Point out each Plasmodium parasite.
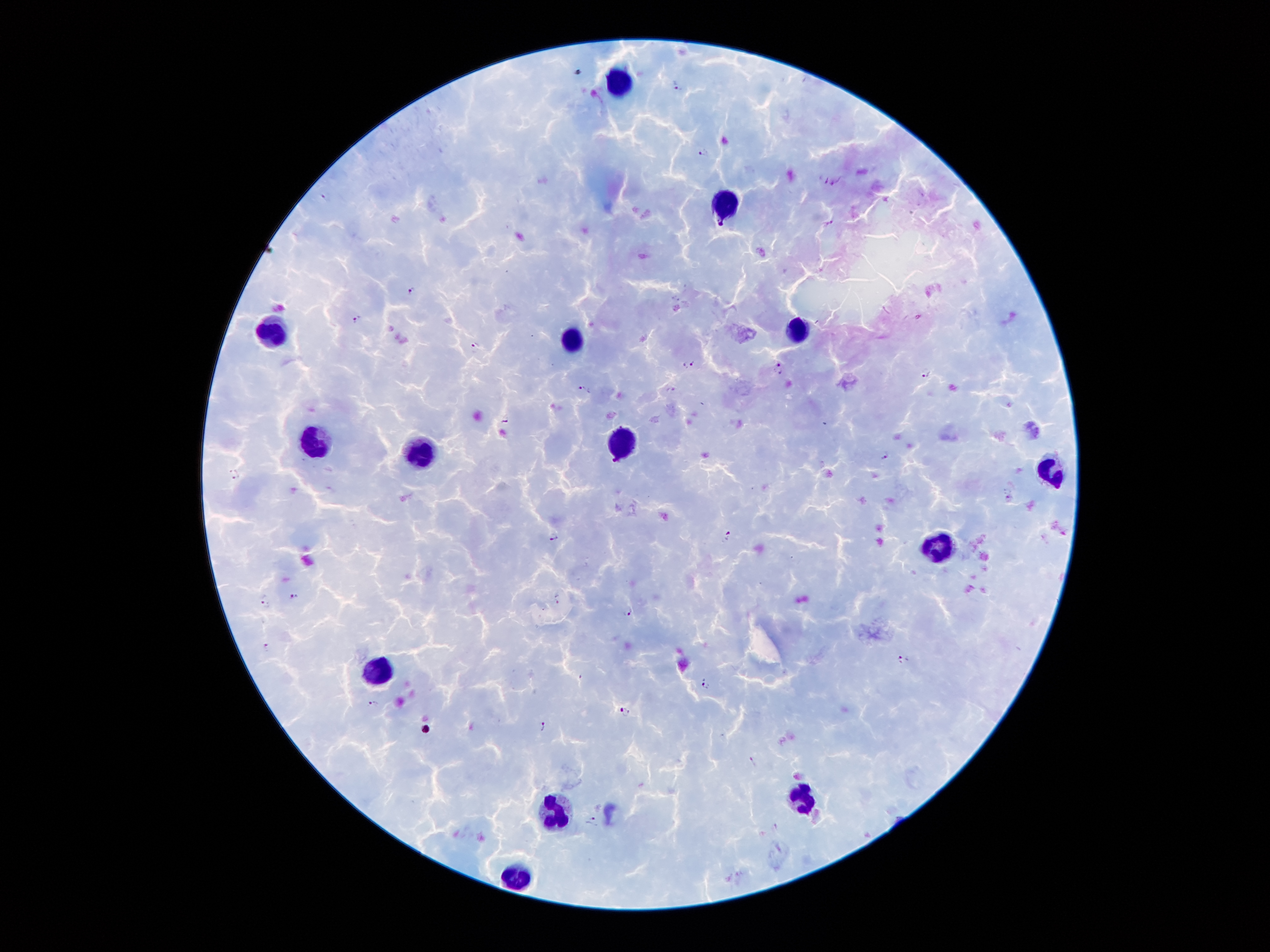

Approximate centers as {x, y} in pixels.
Plasmodium parasites: {676, 84}, {705, 152}, {822, 180}, {835, 182}, {327, 196}, {829, 222}, {411, 291}, {357, 319}, {475, 347}, {689, 364}, {780, 369}, {927, 374}, {584, 389}, {673, 389}, {506, 419}, {885, 455}, {235, 474}, {1009, 498}, {726, 535}, {553, 537}, {294, 596}, {557, 596}, {265, 598}, {628, 610}, {266, 649}, {904, 658}, {707, 684}, {374, 703}, {624, 712}, {542, 727}, {752, 761}, {594, 819}.

Leukocyte locations: {622, 83}, {722, 203}, {795, 330}, {272, 333}, {567, 338}, {311, 442}, {619, 443}, {425, 456}, {1049, 470}, {945, 546}, {377, 671}, {802, 792}, {557, 813}, {518, 875}. Single field of view. Patient malaria status: positive for Plasmodium falciparum. Image is 1270×952 pixels. Thick peripheral-blood smear. Giemsa stain. Smartphone photograph taken through the microscope eyepiece. 100x magnification.